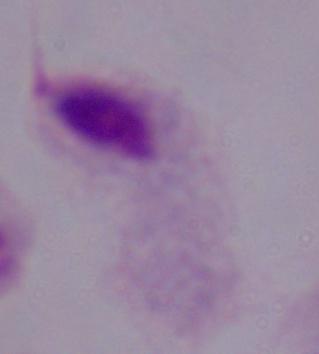 1000x magnification. Photomicrograph. A trichomonad is seen.